Report the malaria status of this cell.
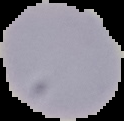

Uninfected.

From a thin blood film. Cell region segmented out of the field of view; the surrounding area is masked to black. Image is 124×121 pixels.